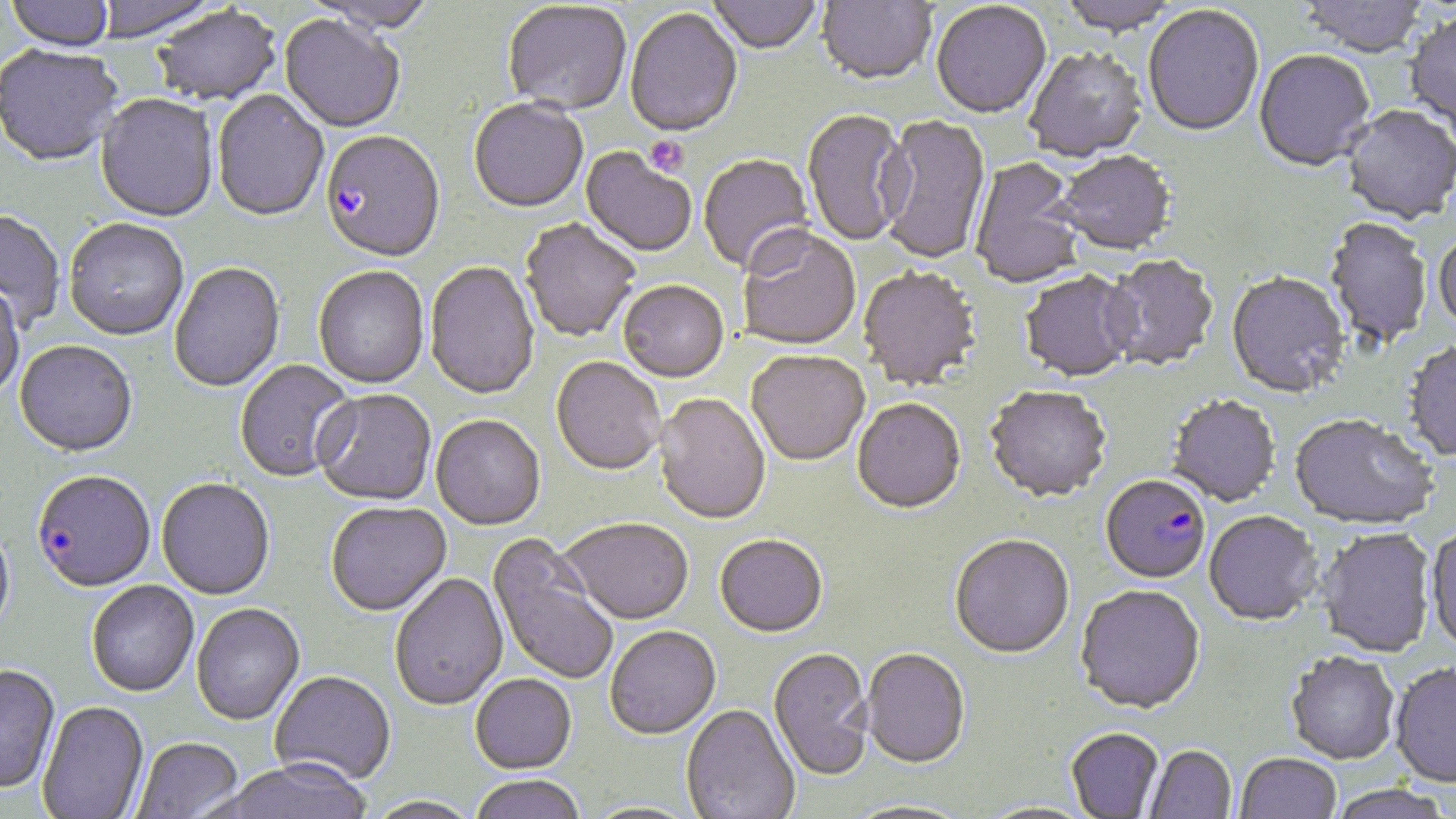

Summary:
  - Coordinate format: approximate bounding boxes as (x1,y1)-(x2,y2) corner pairs in pixels
  - Uninfected red blood cell locations: (6,0)-(115,55), (706,0)-(821,57), (816,0)-(936,88), (1055,0)-(1180,38), (1297,0)-(1429,60), (931,2)-(1052,122), (503,3)-(631,117), (1143,6)-(1264,140), (150,7)-(282,109), (625,9)-(742,140), (1405,15)-(1456,133), (279,16)-(404,135), (0,47)-(122,169), (1024,49)-(1148,163), (1254,52)-(1375,174), (211,91)-(329,224), (95,95)-(219,225), (469,100)-(588,216), (1341,107)-(1455,227), (802,110)-(912,248), (877,115)-(991,266), (580,149)-(696,259), (1054,153)-(1176,257), (698,154)-(815,276), (970,159)-(1088,290), (0,211)-(65,330), (1323,217)-(1433,352), (519,219)-(641,344), (64,220)-(189,342), (737,229)-(861,352), (1433,234)-(1456,336), (1100,256)-(1218,373), (425,262)-(540,402), (170,264)-(285,394), (313,268)-(429,389), (858,268)-(981,392), (1020,273)-(1137,384), (1226,274)-(1350,401), (0,282)-(25,402), (618,282)-(729,384), (1402,342)-(1456,464), (14,343)-(137,459), (747,352)-(870,468), (551,358)-(665,477), (235,361)-(358,483), (985,387)-(1111,505), (314,391)-(437,508), (653,393)-(771,527), (1166,396)-(1281,509), (852,400)-(966,516), (431,417)-(545,532), (1289,418)-(1438,533), (156,479)-(275,602), (326,504)-(452,618), (1204,513)-(1321,628), (0,520)-(16,646), (559,521)-(694,628), (1425,528)-(1456,656), (1315,530)-(1436,659), (486,535)-(619,686), (715,537)-(828,640), (950,537)-(1075,661), (389,574)-(509,711), (86,582)-(199,699), (1075,586)-(1205,717), (191,605)-(305,727), (605,628)-(722,741), (768,649)-(874,782), (861,650)-(970,770), (1285,653)-(1400,767), (1389,664)-(1456,791), (0,666)-(61,796), (270,673)-(396,787), (470,676)-(577,775), (37,702)-(149,819), (680,705)-(800,819), (1066,729)-(1164,817), (132,739)-(244,819), (1144,746)-(1236,819), (1236,754)-(1341,818), (215,764)-(373,819), (469,777)-(585,819), (1328,786)-(1452,819), (364,797)-(484,819), (841,801)-(970,819), (578,802)-(706,819)
  - Platelet locations: (643,136)-(689,178)
  - Plasmodium falciparum-infected red blood cell locations: (321,133)-(445,265), (33,473)-(156,595), (1100,477)-(1210,586)
  - Slide-level diagnosis: Plasmodium falciparum
  - Magnification: 1000x
  - Image size: 1456×819 pixels
  - Stain: May-Grünwald-Giemsa
  - Preparation: thin blood film
  - Field of view: one of a larger specimen
  - Modality: light microscopy